Identify the cell.
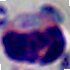

A leukocyte.

{
  "magnification": "1000x",
  "modality": "micrograph"
}